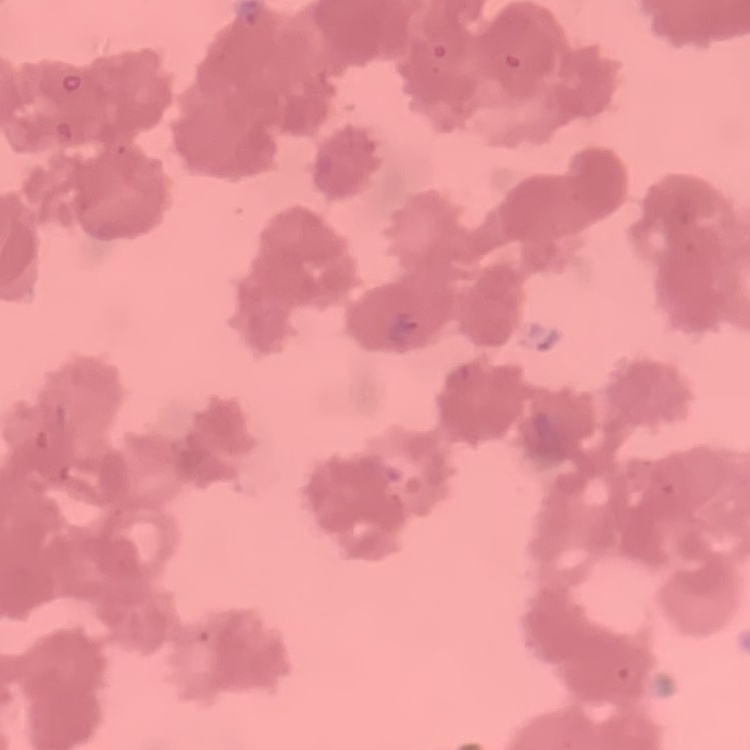

{
  "erythrocyte_morphology": "rouleaux formation",
  "preparation": "thin blood film",
  "stain": "Field's or Giemsa",
  "image_type": "square crop of a larger photomicrograph"
}